Name the cell type shown.
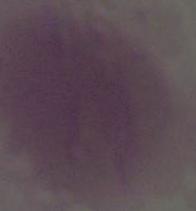
An erythrocyte.

magnification = 1000x
modality = micrograph